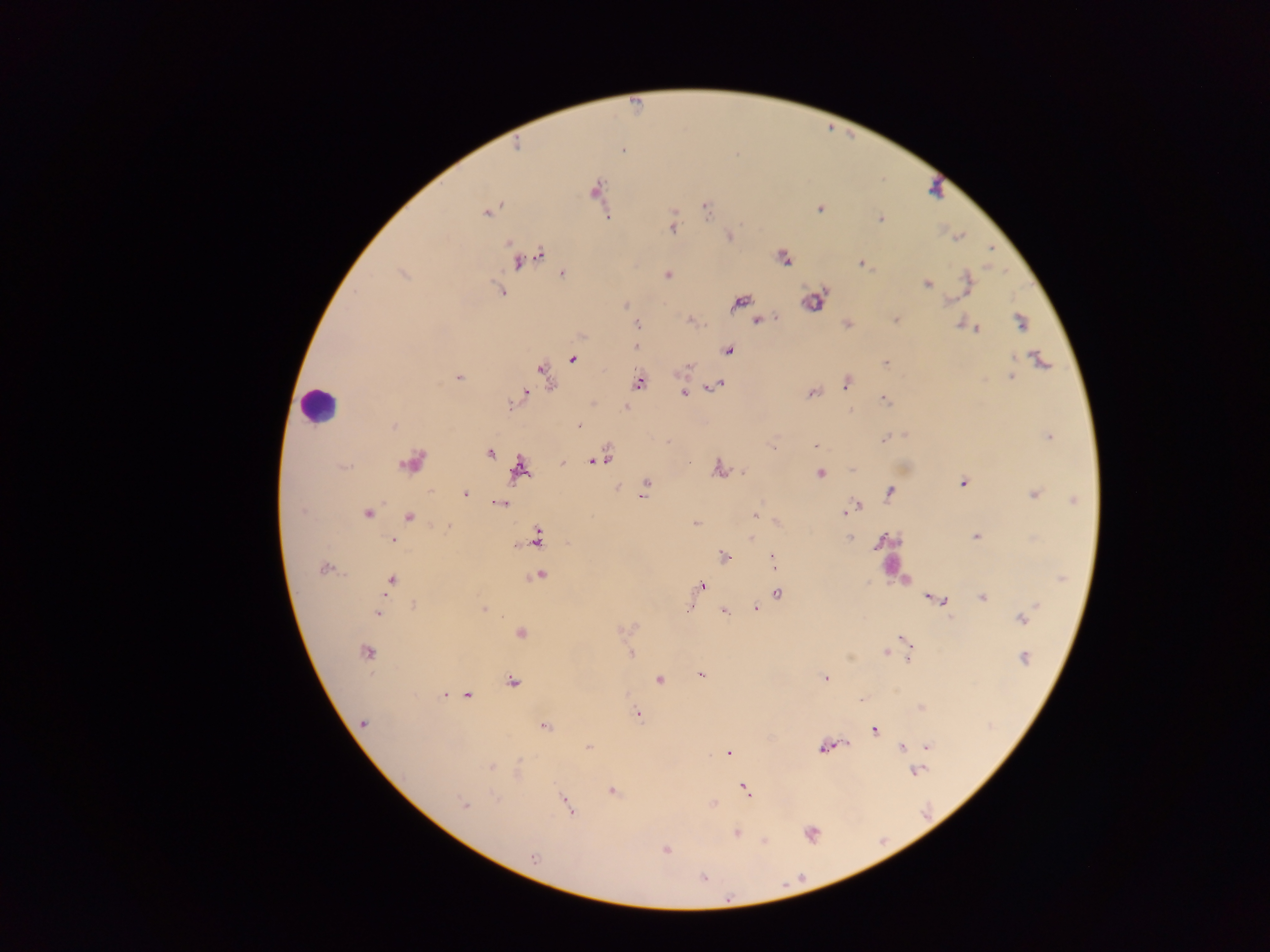

Approximate centers as x y in pixels. Malaria parasite locations: 624 152; 704 207; 819 209; 486 213; 671 214; 612 217; 880 218; 673 225; 729 237; 960 237; 507 243; 990 251; 542 254; 781 256; 517 263; 861 265; 561 272; 966 274; 668 275; 927 283; 968 288; 502 290; 948 298; 625 305; 962 318; 758 319; 689 320; 894 320; 1020 322; 639 324; 846 325; 977 328; 636 345; 728 351; 1038 357; 573 358; 884 362; 689 367; 543 373; 1011 375; 458 377; 640 382; 845 383; 721 384; 713 387; 527 392; 684 392; 810 393; 883 400; 625 407; 578 424; 393 425; 905 433; 1049 435; 884 437; 772 444; 815 445; 489 453; 608 458; 561 463; 591 464; 716 467; 850 469; 743 471; 820 472; 647 482; 961 483; 617 486; 888 492; 465 494; 1033 495; 643 496; 500 503; 859 504; 755 512; 369 514; 845 514; 694 522; 447 527; 975 535; 750 536; 849 536; 392 540; 880 540; 723 557; 773 557; 323 567; 542 575; 390 580; 703 584; 777 592; 925 597; 945 601; 1036 606; 755 607; 690 608; 485 609; 723 611; 378 613; 1021 620; 621 630; 520 632; 899 638; 630 653; 885 653; 850 656; 1023 657; 702 675; 825 677; 660 679; 513 683; 468 693; 443 695; 861 700; 639 714; 364 724; 545 725; 876 731; 844 744; 589 747; 902 747; 927 747; 820 748; 727 754; 520 761; 492 767; 612 789; 748 793; 495 797; 712 804; 466 805; 569 808; 737 833; 764 840; 666 850; 534 857. Leukocyte locations: 322 407. Collected in Ghana. Photographed through a microscope with a mobile-phone camera. One field of view. Image is 1270×952 pixels. Thick blood film.